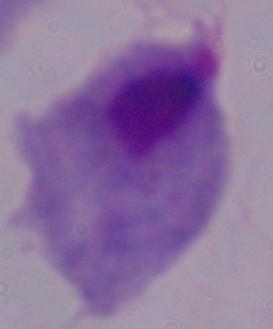

A trichomonad is shown. Captured at 1000x magnification. Photomicrograph.